Name the cell type shown.
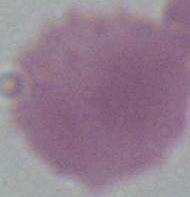

This is an erythrocyte.

1000x magnification. Photomicrograph.